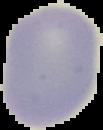
From a thin blood smear. Malaria status: uninfected. The area outside the segmented cell region is set to black. Image is 103×130 pixels.